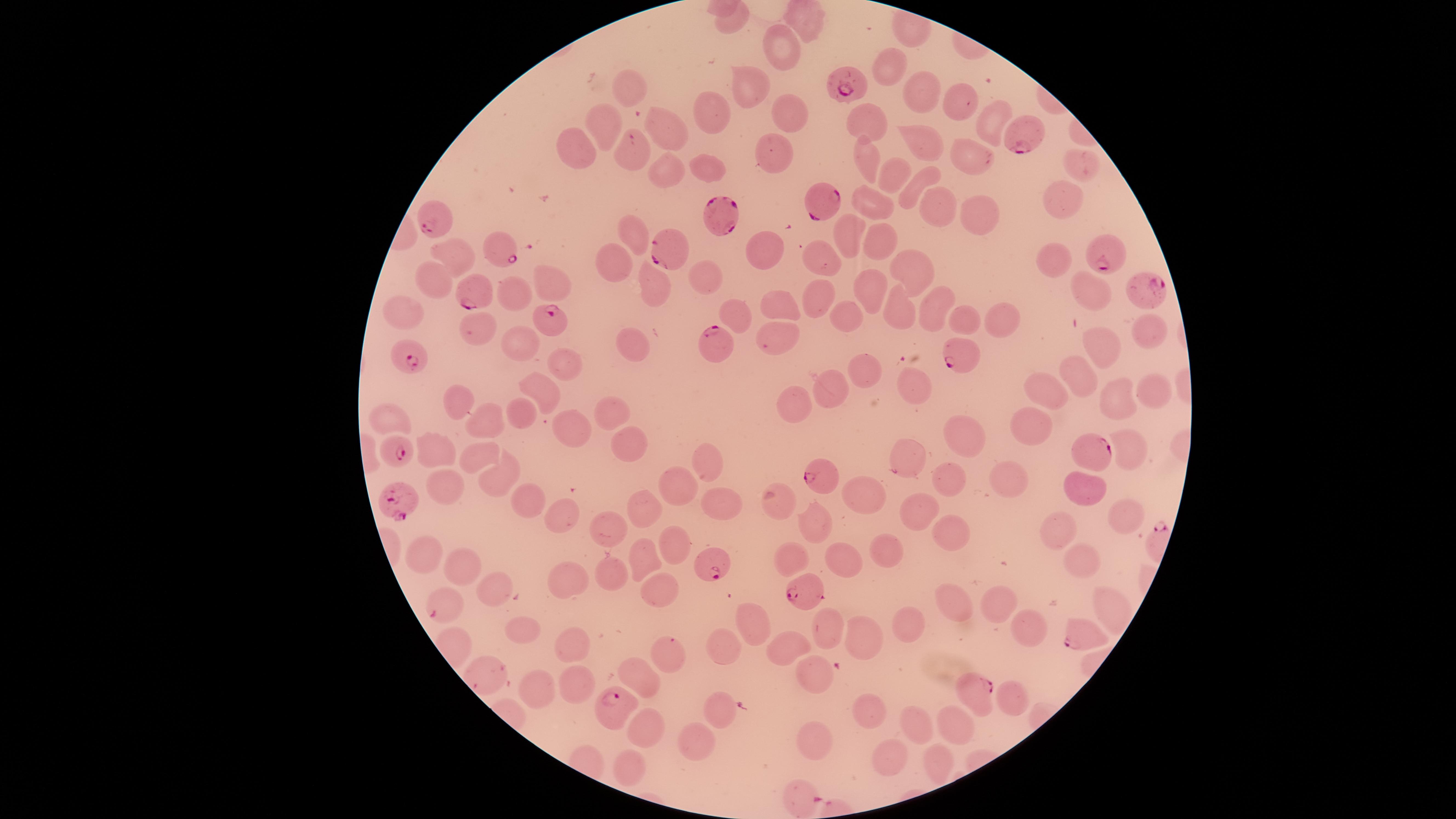

Approximate marker points as [x, y] in pixels.
Summary:
  - Uninfected RBCs: [784, 39], [890, 66], [743, 82], [628, 86], [916, 90], [964, 93], [789, 111], [708, 113], [990, 115], [865, 122], [603, 128], [671, 134], [922, 140], [576, 145], [775, 149], [971, 149], [864, 157], [1083, 163], [708, 167], [666, 171], [890, 174], [909, 186], [878, 197], [1061, 197], [940, 204], [979, 214], [635, 228], [851, 233], [876, 235], [758, 248], [450, 252], [829, 253], [1057, 257], [616, 259], [904, 265], [706, 275], [552, 280], [867, 281], [431, 285], [1097, 290], [656, 292], [512, 297], [816, 297], [941, 301], [785, 302], [898, 304], [737, 307], [405, 311], [847, 312], [965, 316], [997, 319], [476, 329], [1150, 333], [773, 341], [1108, 343], [629, 344], [520, 348], [566, 362], [858, 365], [1083, 370], [915, 384], [826, 387], [1055, 387], [1157, 389], [456, 393], [544, 395], [1118, 398], [796, 403], [522, 407], [614, 409], [391, 418], [483, 418], [1039, 423], [573, 427], [967, 429], [1129, 443], [436, 445], [631, 447], [904, 453], [476, 458], [706, 460], [500, 476], [948, 476], [1018, 476], [437, 478], [682, 482], [1081, 488], [523, 500], [721, 501], [869, 509], [642, 510], [558, 513], [924, 517], [1120, 519], [814, 523], [949, 527], [609, 528], [1062, 528], [675, 541], [416, 547], [890, 550], [1085, 554], [643, 556], [797, 559], [844, 565], [463, 566], [609, 573], [571, 577], [660, 586], [495, 587], [959, 600], [999, 611], [753, 620], [900, 624], [518, 625], [1024, 630], [830, 636], [866, 642], [571, 646], [787, 647], [725, 649], [660, 652], [642, 671], [816, 679], [577, 689], [534, 693], [1013, 694], [720, 708], [869, 716], [917, 725], [959, 726], [642, 727], [697, 738], [812, 745], [895, 755], [943, 763], [627, 766]
  - Parasitized RBCs: [849, 85], [1027, 135], [631, 137], [822, 198], [724, 217], [437, 221], [1099, 248], [499, 252], [668, 253], [1150, 289], [470, 291], [549, 317], [713, 342], [405, 357], [964, 358], [397, 451], [1099, 454], [822, 479], [403, 504], [710, 560], [804, 593], [435, 613], [1077, 636], [974, 686], [614, 705], [798, 796]
  - Visible region: circular
  - Preparation: thin smear of blood
  - Image size: 1456×819 pixels
  - Capture: smartphone photograph through the microscope eyepiece
  - Stain: Giemsa
  - Field of view: single
  - Species: Plasmodium falciparum
  - Presence: malaria parasites seen